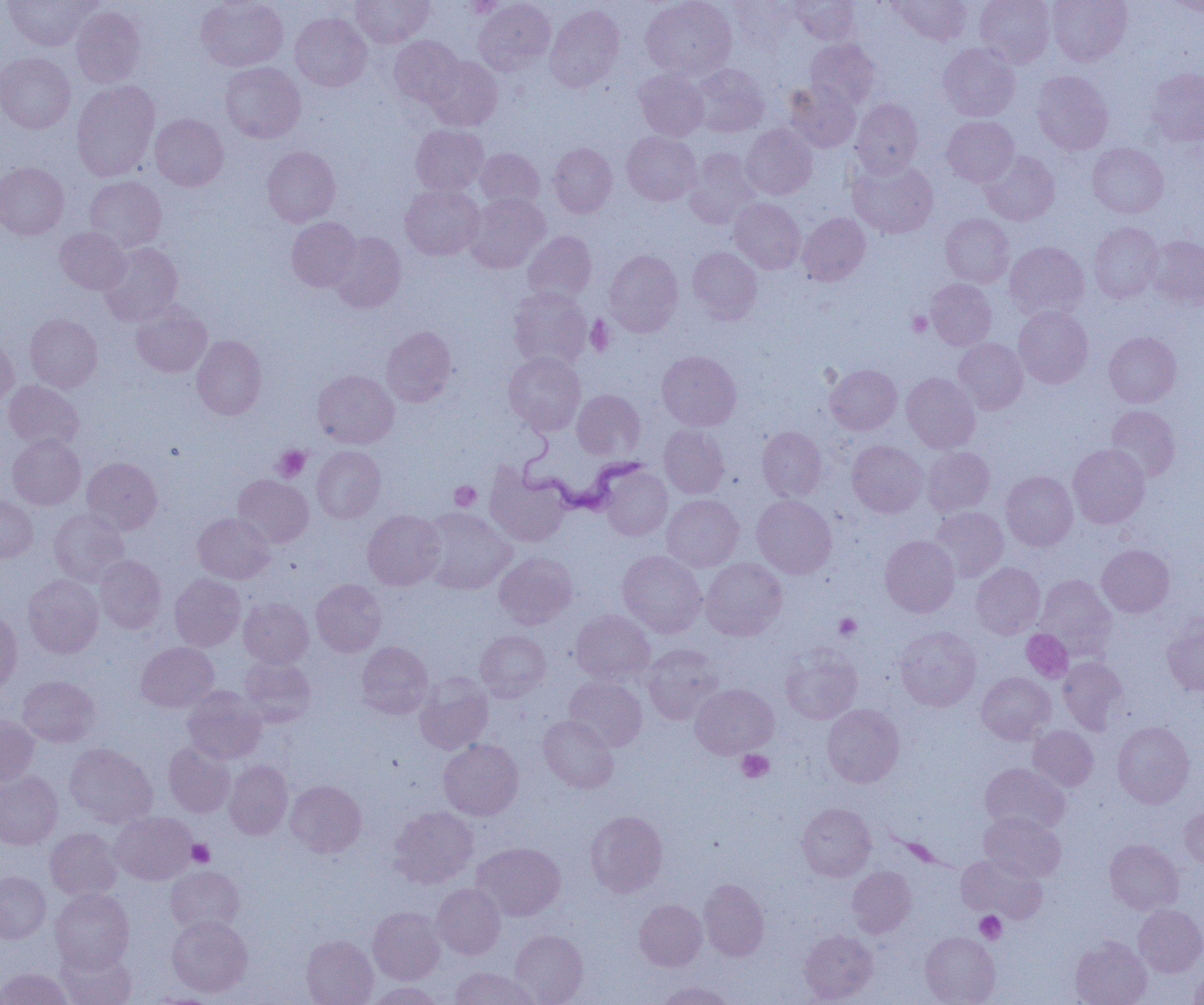

slide_level_diagnosis: Trypanosoma brucei
preparation: thin blood smear
uninfected_red_blood_cell_locations_subset: 'approximate bounding boxes as [x1, y1, x2, y2] in pixels: [196, 0, 288, 71], [351, 0, 434, 47], [473, 0, 555, 75], [641, 0, 737, 80], [728, 0, 801, 49], [790, 0, 861, 45], [891, 0, 972, 45], [975, 0, 1055, 67], [1048, 0, 1132, 66], [1165, 0, 1204, 17], [3, 1, 96, 50], [545, 4, 625, 91], [71, 6, 145, 88], [290, 13, 371, 91], [388, 35, 464, 107], [805, 38, 880, 109], [938, 43, 1019, 121], [0, 52, 76, 133], [424, 56, 503, 131], [221, 62, 305, 143], [691, 64, 769, 137], [1145, 67, 1204, 145], [634, 69, 708, 141], [1031, 71, 1113, 154], [71, 80, 160, 181], [784, 82, 861, 152], [851, 99, 923, 177], [150, 113, 228, 190], [942, 116, 1019, 186], [411, 124, 489, 195], [741, 124, 817, 199], [622, 132, 701, 206], [549, 143, 618, 218], [1087, 143, 1168, 217], [262, 146, 340, 226], [476, 148, 544, 210], [685, 148, 761, 228], [980, 150, 1060, 225], [848, 158, 938, 238], [0, 162, 68, 239], [84, 176, 167, 252], [400, 184, 484, 260], [465, 193, 550, 272], [730, 198, 805, 274], [798, 212, 870, 286], [940, 214, 1014, 287], [286, 217, 361, 291], [1088, 222, 1162, 302], [55, 227, 130, 294], [523, 231, 597, 304], [329, 232, 406, 313], [1145, 234, 1204, 309], [1005, 241, 1089, 320], [98, 242, 183, 326], [688, 247, 762, 323], [605, 249, 683, 336], [926, 278, 996, 350], [508, 287, 592, 370], [131, 301, 212, 377], [1013, 306, 1093, 388], [25, 314, 103, 392], [381, 326, 457, 406], [1104, 332, 1181, 407], [0, 334, 19, 410], [192, 335, 267, 420], [954, 338, 1028, 414], [657, 351, 741, 431], [504, 352, 586, 434], [825, 364, 901, 434], [312, 370, 399, 448], [902, 373, 980, 452], [3, 380, 83, 451], [572, 389, 645, 461], [1107, 406, 1180, 481], [658, 425, 729, 498], [757, 427, 827, 501], [7, 434, 86, 510], [847, 440, 928, 517], [1068, 444, 1150, 528], [312, 446, 385, 523], [923, 447, 995, 516], [82, 457, 162, 534], [485, 466, 570, 547], [600, 466, 673, 540], [1001, 471, 1078, 551], [233, 475, 314, 548], [661, 494, 744, 571], [752, 494, 837, 578], [0, 495, 37, 563], [420, 507, 515, 594], [930, 507, 1008, 581], [49, 509, 129, 586], [363, 510, 445, 589], [192, 513, 274, 583], [880, 535, 960, 617], [1097, 544, 1174, 617], [617, 550, 707, 638], [494, 552, 577, 629], [95, 555, 166, 633], [701, 558, 787, 640], [971, 562, 1045, 638], [169, 573, 245, 651], [23, 575, 103, 658], [1036, 575, 1116, 658], [311, 579, 386, 656], [239, 597, 314, 668], [571, 609, 655, 686], [0, 610, 22, 698], [1162, 615, 1204, 695], [895, 626, 981, 711], [475, 630, 551, 701], [357, 641, 433, 718], [136, 642, 218, 712], [643, 644, 723, 724], [780, 647, 861, 723], [239, 656, 316, 727], [1057, 657, 1128, 734], [976, 672, 1055, 744], [17, 675, 100, 747], [414, 675, 493, 754], [563, 676, 647, 751], [690, 683, 778, 758], [182, 686, 266, 764], [822, 704, 904, 787], [0, 714, 39, 787], [538, 715, 619, 792], [1112, 721, 1194, 808], [1028, 725, 1098, 791], [438, 739, 523, 820], [163, 742, 235, 818], [64, 743, 157, 827], [224, 760, 293, 839], [980, 763, 1069, 835], [0, 771, 62, 850], [285, 780, 366, 857], [797, 803, 876, 881], [388, 806, 478, 888], [1180, 806, 1204, 869], [585, 810, 667, 897], [111, 811, 197, 885], [979, 812, 1065, 882], [45, 828, 122, 900], [1105, 839, 1183, 915], [471, 842, 565, 921], [956, 854, 1046, 923], [165, 865, 245, 935], [847, 866, 916, 937], [0, 871, 50, 943], [698, 879, 769, 961], [432, 883, 505, 959], [50, 887, 135, 973], [634, 899, 707, 971], [1133, 904, 1204, 977], [368, 906, 445, 984], [167, 915, 253, 997], [799, 929, 877, 1003], [509, 930, 588, 1004], [920, 931, 1000, 1005], [301, 934, 378, 1005], [1070, 936, 1151, 1005], [57, 946, 136, 1005], [1190, 963, 1204, 1004], [449, 966, 539, 1005], [1, 967, 72, 1005], [654, 981, 735, 1005], [366, 982, 444, 1005], [148, 993, 226, 1005]'
magnification: 1000x
image_size: 1204×1005 pixels
platelet_locations_subset: 'approximate bounding boxes as [x1, y1, x2, y2] in pixels: [907, 311, 933, 336], [585, 316, 615, 356], [273, 445, 311, 482], [449, 480, 481, 511], [834, 613, 861, 639], [737, 750, 774, 783], [188, 839, 214, 866], [974, 911, 1006, 943]'
modality: optical microscopy
trypanosoma_brucei_locations: 'approximate bounding boxes as [x1, y1, x2, y2] in pixels: [513, 430, 650, 519]'
field_of_view: single